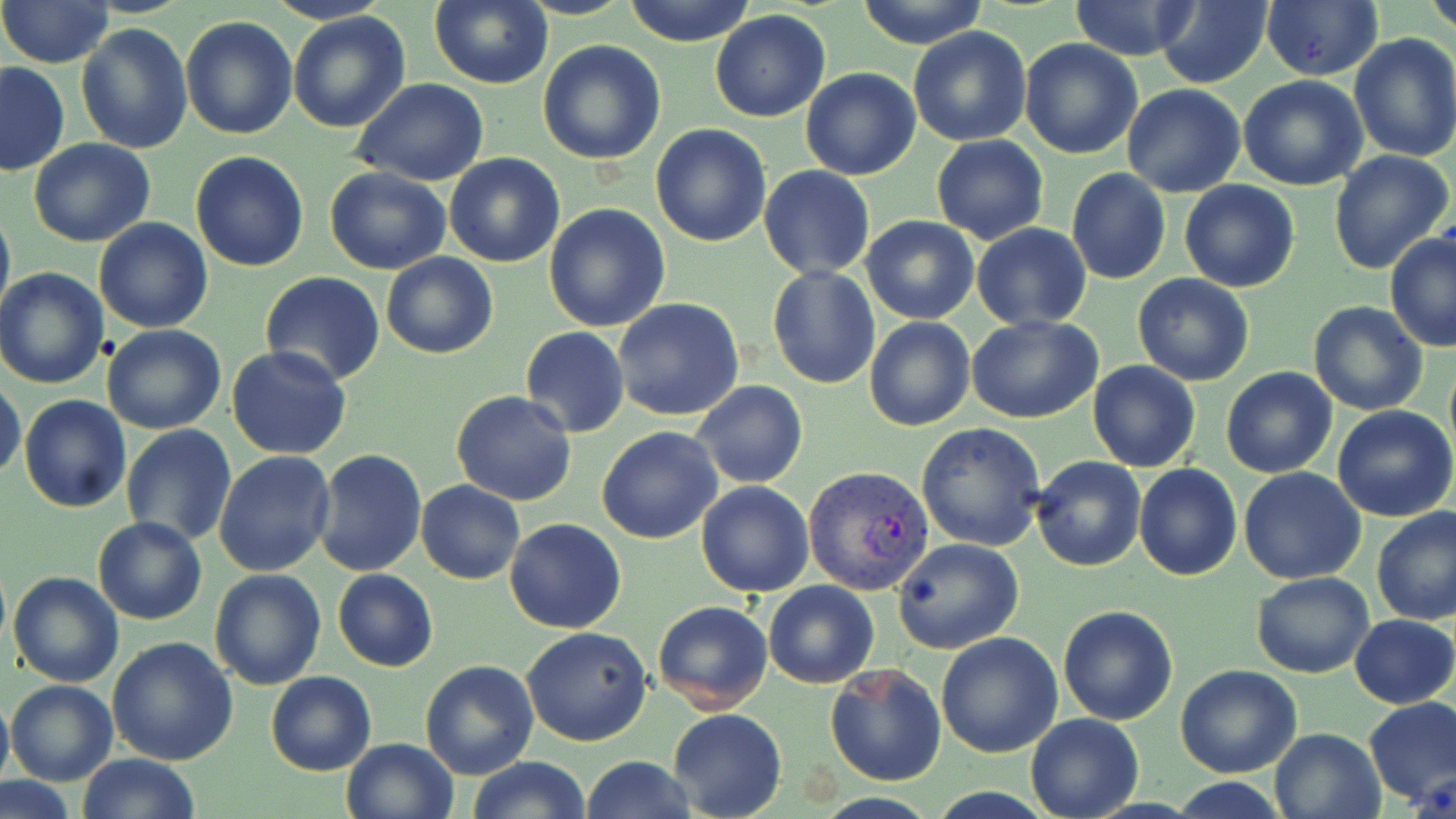

slide-level diagnosis = Plasmodium vivax
magnification = 1000x
modality = optical microscopy
uninfected red blood cell locations = approximate bounding boxes as (x1, y1, x2, y2) in pixels: (0, 0, 116, 69), (264, 0, 391, 26), (623, 0, 757, 47), (855, 0, 991, 49), (1425, 0, 1456, 37), (428, 1, 553, 89), (1066, 1, 1205, 61), (1153, 2, 1274, 88), (1260, 2, 1384, 81), (288, 10, 413, 133), (709, 11, 831, 122), (180, 16, 297, 140), (76, 23, 191, 153), (909, 26, 1032, 147), (1349, 33, 1456, 163), (537, 39, 666, 166), (1019, 39, 1144, 159), (0, 61, 70, 176), (801, 68, 920, 181), (1238, 75, 1369, 190), (352, 77, 489, 186), (1122, 85, 1248, 198), (650, 123, 774, 248), (931, 135, 1049, 244), (28, 137, 155, 247), (1329, 150, 1453, 276), (189, 151, 309, 272), (444, 153, 566, 267), (325, 164, 452, 275), (758, 166, 875, 279), (1066, 168, 1170, 285), (1179, 180, 1300, 293), (0, 202, 14, 324), (544, 202, 671, 334), (859, 214, 979, 325), (94, 218, 213, 333), (969, 223, 1091, 330), (1385, 232, 1456, 352), (382, 252, 497, 359), (767, 265, 881, 389), (0, 268, 109, 390), (259, 272, 385, 387), (1131, 273, 1254, 386), (612, 298, 744, 422), (1308, 300, 1429, 417), (967, 314, 1102, 423), (865, 317, 975, 432), (103, 324, 228, 435), (519, 326, 629, 437), (225, 346, 352, 461), (1086, 360, 1201, 472), (1221, 367, 1337, 479), (0, 377, 26, 482), (691, 381, 808, 489), (451, 391, 578, 507), (21, 396, 132, 512), (1332, 405, 1455, 522), (916, 422, 1046, 551), (120, 425, 237, 548), (596, 426, 724, 544), (312, 448, 427, 576), (213, 449, 337, 577), (1030, 456, 1146, 573), (1134, 464, 1241, 581), (1238, 467, 1368, 584), (416, 480, 525, 584), (696, 481, 815, 598), (1371, 507, 1456, 626), (93, 516, 206, 624), (504, 517, 627, 634), (892, 537, 1024, 654), (207, 568, 327, 690), (331, 568, 439, 672), (8, 572, 124, 689), (1251, 572, 1374, 677), (763, 579, 879, 689), (651, 600, 775, 716), (1057, 604, 1179, 725), (1350, 614, 1456, 708), (520, 627, 652, 747), (935, 632, 1062, 758), (106, 636, 239, 766), (421, 660, 538, 780), (824, 662, 945, 786), (1175, 664, 1302, 779), (266, 672, 377, 775), (7, 679, 117, 786), (0, 687, 12, 796), (1362, 696, 1456, 807), (668, 709, 786, 819), (1025, 712, 1142, 818), (1268, 728, 1385, 818), (340, 738, 460, 819), (75, 753, 202, 818), (582, 755, 697, 819), (467, 756, 591, 819), (0, 777, 76, 819)
image size = 1456×819 pixels
Plasmodium vivax-infected red blood cell locations = approximate bounding boxes as (x1, y1, x2, y2) in pixels: (803, 467, 934, 594)
preparation = thin blood film
stain = May-Grünwald-Giemsa
field of view = single